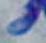

Toxoplasma gondii is seen. Photomicrograph. 1000x magnification.